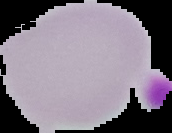
preparation = thin blood film
image size = 172×133 pixels
image type = cell region segmented out of the field of view; surrounding area masked to black
malaria status = uninfected